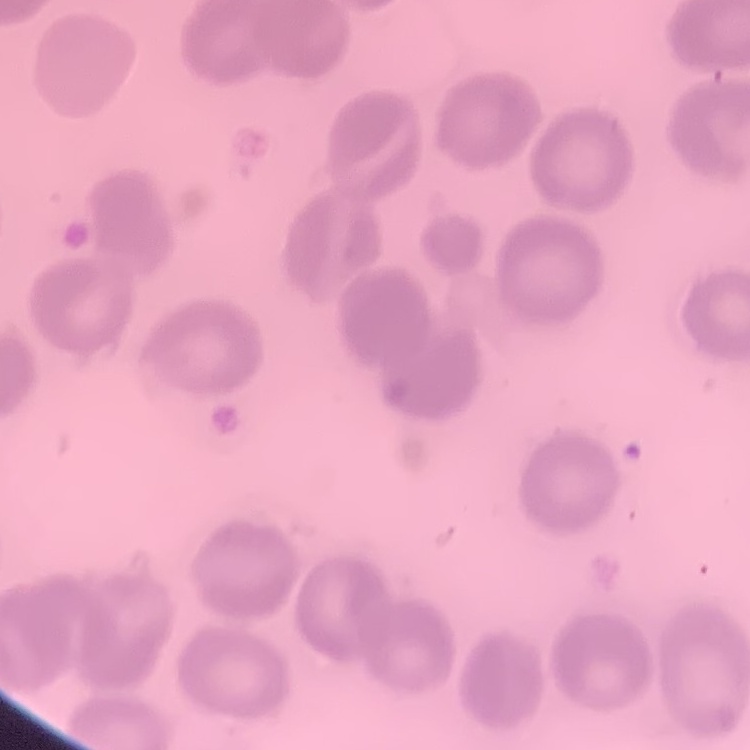
red_blood_cell_morphology: no rouleaux formation
image_type: one tile cut from a larger photomicrograph
stain: Field's or Giemsa
preparation: thin peripheral smear